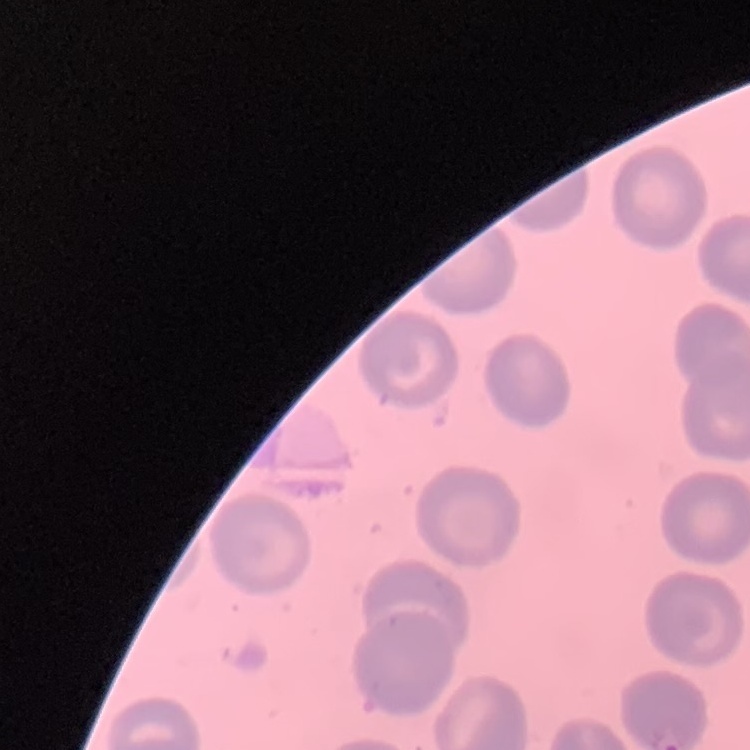
The red blood cells show no rouleaux formation. Thin blood smear. One tile cut from a larger photomicrograph. Field's or Giemsa stain.